Identify the parasite.
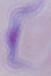

A trypanosome.

1000x magnification. Photomicrograph.